Identify the blood parasite species.
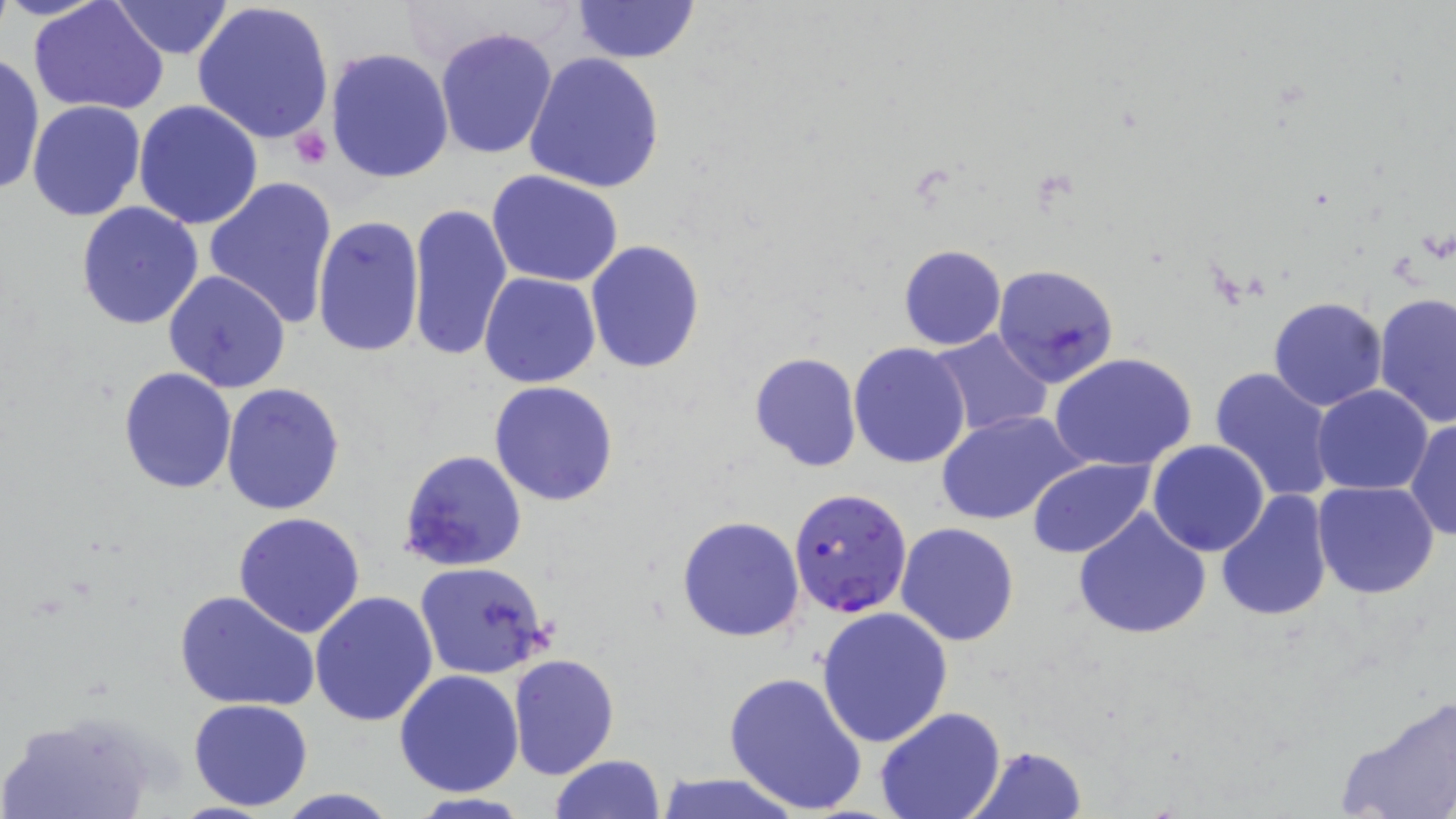
Plasmodium falciparum.

Approximate bounding boxes as named x1/y1/x2/y2 corners in pixels. Uninfected red blood cell locations: (x1=29, y1=0, x2=168, y2=116), (x1=108, y1=0, x2=237, y2=60), (x1=190, y1=0, x2=336, y2=146), (x1=569, y1=0, x2=702, y2=65), (x1=435, y1=27, x2=559, y2=160), (x1=325, y1=47, x2=454, y2=183), (x1=0, y1=52, x2=45, y2=195), (x1=524, y1=52, x2=665, y2=194), (x1=26, y1=100, x2=145, y2=220), (x1=133, y1=100, x2=264, y2=229), (x1=486, y1=171, x2=626, y2=289), (x1=203, y1=175, x2=340, y2=331), (x1=75, y1=202, x2=205, y2=331), (x1=406, y1=202, x2=512, y2=362), (x1=312, y1=214, x2=426, y2=361), (x1=585, y1=241, x2=704, y2=373), (x1=898, y1=245, x2=1006, y2=350), (x1=992, y1=263, x2=1121, y2=388), (x1=162, y1=269, x2=290, y2=392), (x1=479, y1=271, x2=600, y2=387), (x1=1374, y1=293, x2=1456, y2=427), (x1=1269, y1=297, x2=1388, y2=412), (x1=927, y1=329, x2=1054, y2=438), (x1=847, y1=341, x2=972, y2=469), (x1=748, y1=352, x2=862, y2=473), (x1=1049, y1=352, x2=1199, y2=473), (x1=117, y1=367, x2=238, y2=495), (x1=1209, y1=367, x2=1336, y2=505), (x1=489, y1=379, x2=620, y2=506), (x1=222, y1=383, x2=345, y2=517), (x1=1312, y1=386, x2=1432, y2=495), (x1=937, y1=410, x2=1084, y2=526), (x1=1406, y1=415, x2=1456, y2=542), (x1=1148, y1=440, x2=1269, y2=555), (x1=398, y1=449, x2=526, y2=571), (x1=1027, y1=458, x2=1154, y2=559), (x1=1312, y1=481, x2=1440, y2=600), (x1=1216, y1=491, x2=1332, y2=624), (x1=1073, y1=508, x2=1210, y2=640), (x1=233, y1=512, x2=366, y2=639), (x1=677, y1=516, x2=805, y2=642), (x1=896, y1=523, x2=1019, y2=645), (x1=414, y1=561, x2=552, y2=680), (x1=174, y1=589, x2=318, y2=713), (x1=310, y1=590, x2=438, y2=726), (x1=815, y1=606, x2=953, y2=747), (x1=507, y1=653, x2=620, y2=780), (x1=394, y1=669, x2=524, y2=796), (x1=722, y1=670, x2=868, y2=815), (x1=1338, y1=693, x2=1456, y2=819), (x1=187, y1=698, x2=314, y2=812), (x1=874, y1=707, x2=1005, y2=819), (x1=0, y1=708, x2=161, y2=819), (x1=966, y1=745, x2=1088, y2=819), (x1=549, y1=755, x2=666, y2=818), (x1=652, y1=774, x2=806, y2=818), (x1=270, y1=790, x2=404, y2=819). Platelet locations: (x1=291, y1=127, x2=333, y2=170). Plasmodium falciparum-infected red blood cell locations: (x1=788, y1=487, x2=912, y2=619). Image is 1456×819 pixels. May-Grünwald-Giemsa-stained preparation. One field of a larger specimen. Light microscopy. Captured at 1000x magnification. Thin blood smear.